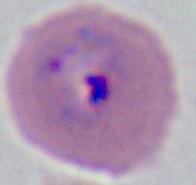

identification = Plasmodium
modality = photomicrograph
magnification = 400x or 1000x